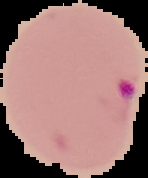

From a thin blood film. Segmented cell region on a black background. Malaria status: parasitized. Image is 148×178 pixels.